Comment on the morphology of the erythrocytes.
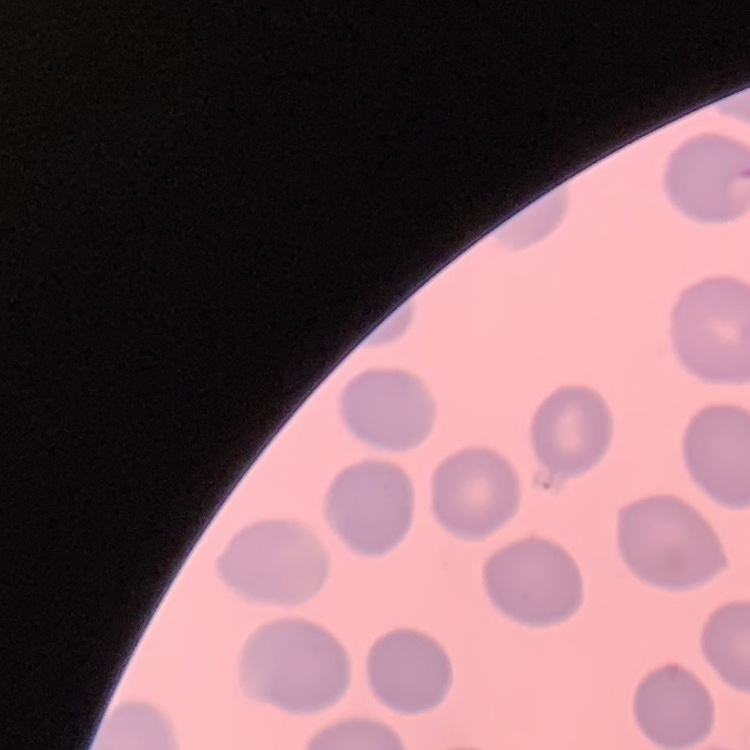
No rouleaux formation.

Square crop of a larger photomicrograph. Stained with either Field's or Giemsa. Thin peripheral smear.